Give the preparation type.
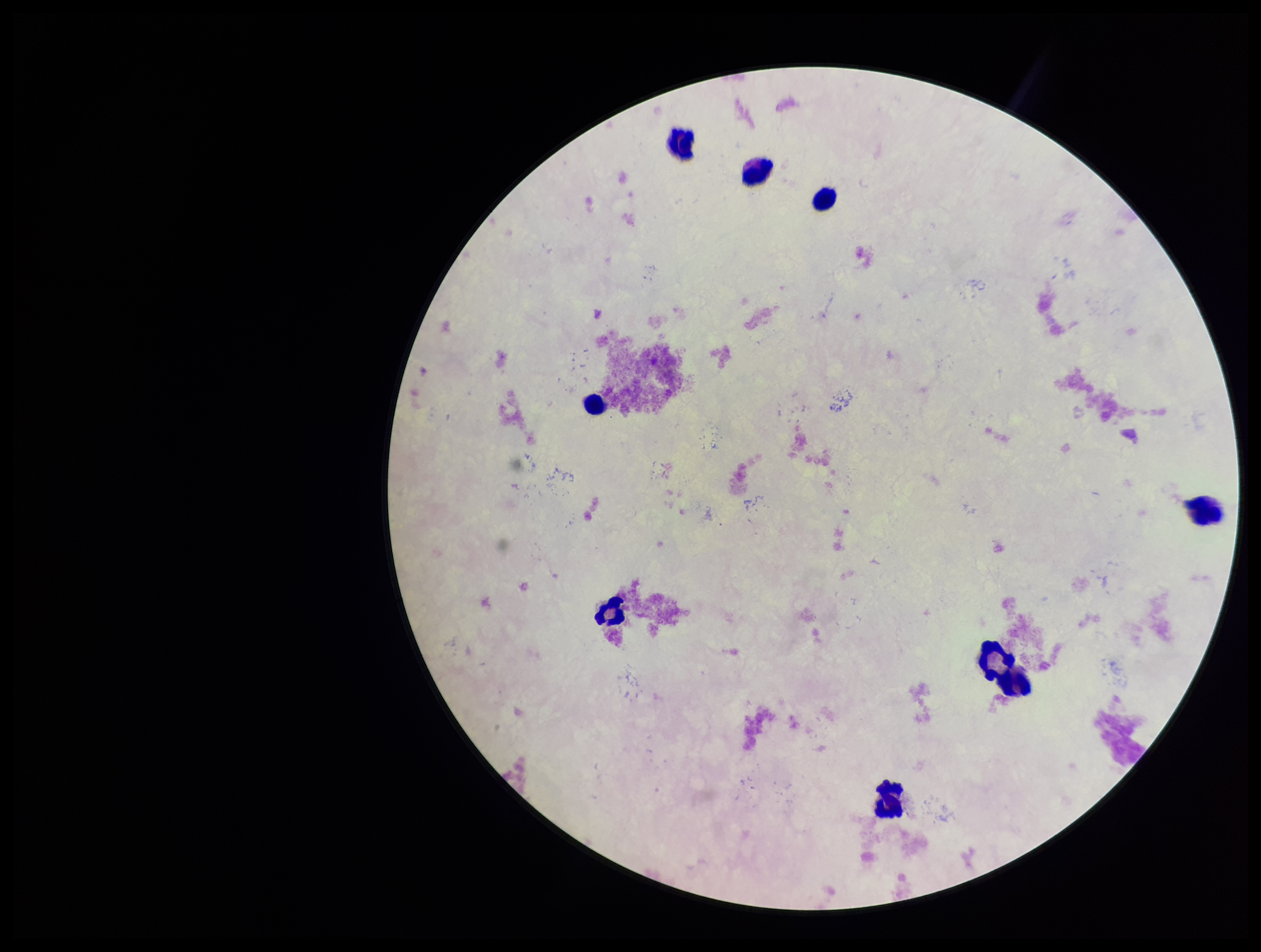

It is a thick blood smear.

parasite_count: 0
stain: Giemsa
plasmodium_parasites: none detected
field_of_view: one from this slide
patient_malaria_status: negative
leukocyte_count: 8
capture: smartphone photograph through the microscope eyepiece
image_size: 1261×952 pixels